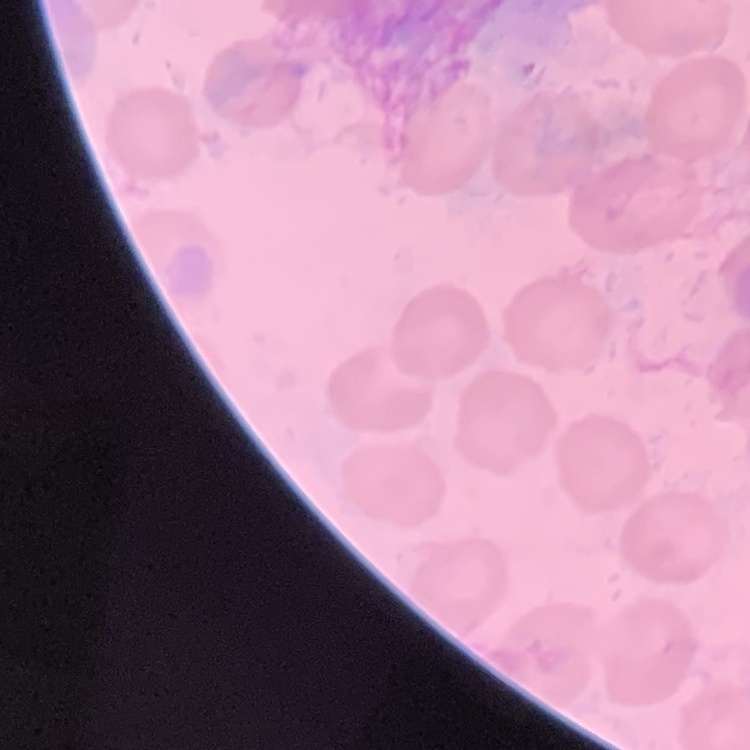
erythrocyte morphology = no rouleaux formation
preparation = thin blood film
image type = one tile cut from a larger photomicrograph
stain = Field's or Giemsa